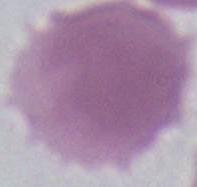

1000x magnification. Micrograph. A red blood cell is seen.